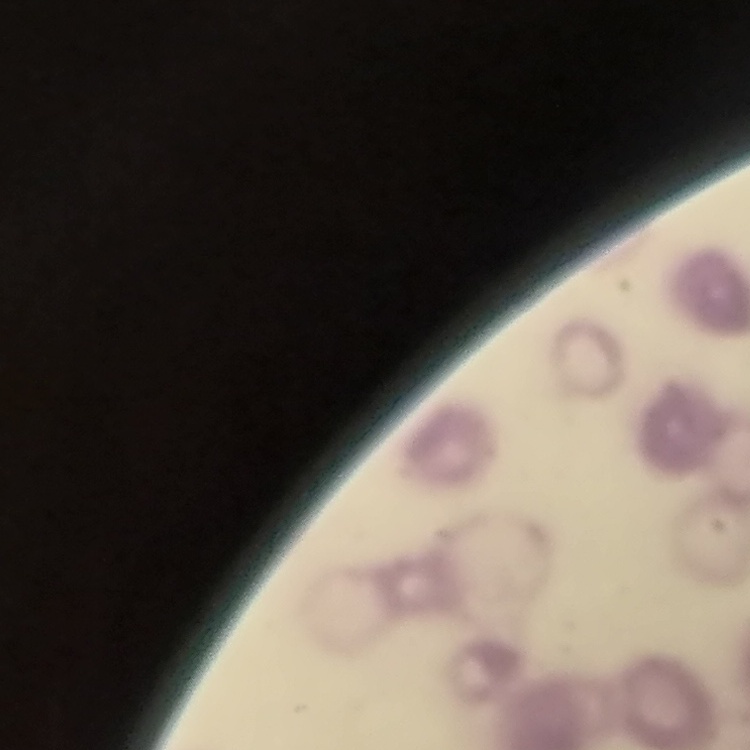
{
  "red_blood_cell_morphology": "rouleaux formation",
  "stain": "Field's or Giemsa",
  "image_type": "one tile cut from a larger photomicrograph",
  "preparation": "thin blood smear"
}